Classify this cell by malaria status.
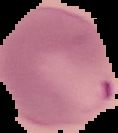

It is parasitized.

Summary:
  - Image type: segmented cell region on a black background
  - Image size: 118×133 pixels
  - Preparation: thin blood smear